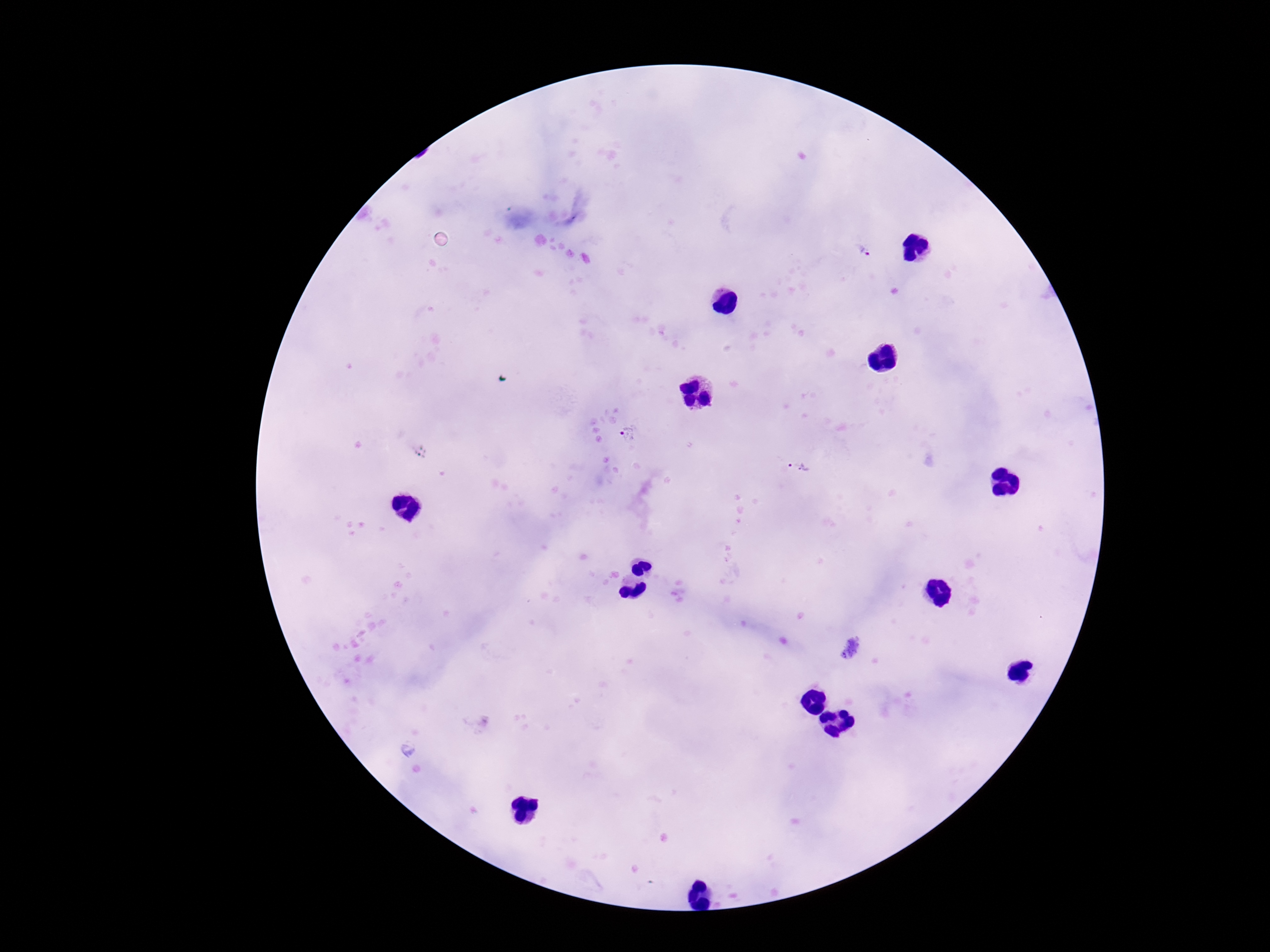

Approximate centers as [x, y] in pixels.
Summary:
  - Plasmodium parasite locations: [864, 250], [629, 434], [798, 467]
  - Field of view: single
  - Patient malaria status: infected
  - Capture: smartphone camera through the microscope eyepiece
  - Preparation: thick blood film
  - Image size: 1270×952 pixels
  - Magnification: 100x
  - Stain: Giemsa